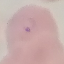

Summary:
  - Malaria status: parasitized
  - Capture: smartphone through the microscope eyepiece
  - Image type: automatically extracted cell patch, resized to 64 × 64 pixels
  - Preparation: thin blood film
  - Stain: Giemsa